Report the malaria status of this cell.
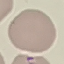

It is uninfected.

capture = smartphone camera at the microscope eyepiece
preparation = thin blood smear
image type = automatically extracted cell patch, resized to 64 × 64 pixels
stain = Giemsa